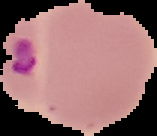

Segmented cell region on a black background. Image is 157×136 pixels. Malaria status: parasitized. From a thin blood smear.